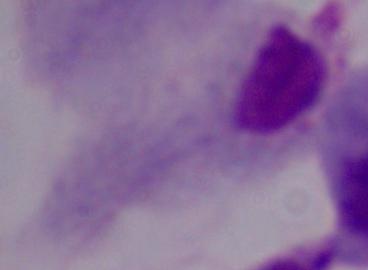
magnification: 1000x
modality: micrograph
identification: trichomonad